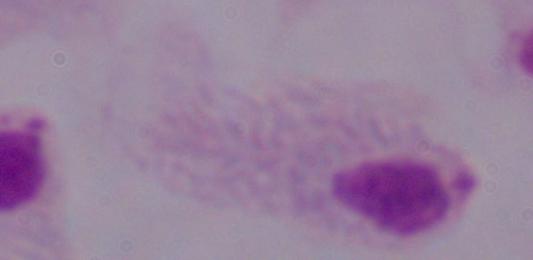
{
  "modality": "micrograph",
  "identification": "trichomonad",
  "magnification": "1000x"
}